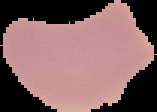
Summary:
  - Image type: segmented cell region with the area outside set to black
  - Preparation: thin blood film
  - Malaria status: uninfected
  - Image size: 157×112 pixels